Report the malaria status of this cell.
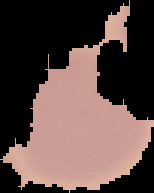

It is uninfected.

Summary:
  - Image type: segmented cell region with the area outside set to black
  - Image size: 154×193 pixels
  - Preparation: thin blood smear